Assess the morphology of the erythrocytes.
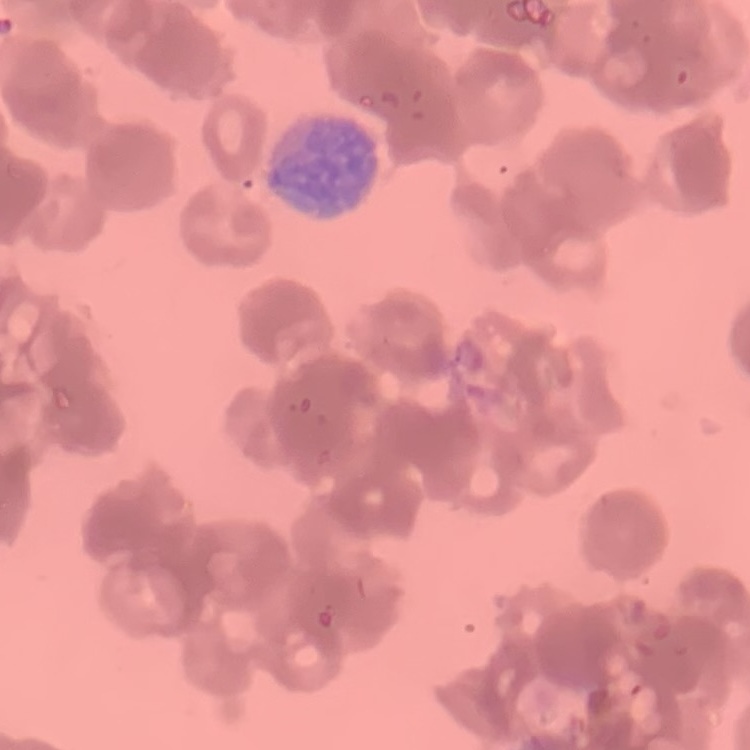

Rouleaux formation.

Stained with either Field's or Giemsa. Thin blood smear. Square crop of a larger photomicrograph.